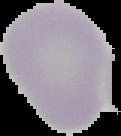
Summary:
  - Image type: cell region segmented out of the field of view; surrounding area masked to black
  - Preparation: thin blood smear
  - Image size: 121×136 pixels
  - Result: negative for Plasmodium parasites